Assess this cell for malaria.
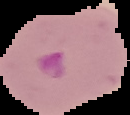

Parasitized.

Summary:
  - Image size: 130×115 pixels
  - Image type: segmented cell region with the area outside set to black
  - Preparation: thin blood smear